Comment on the morphology of the red blood cells.
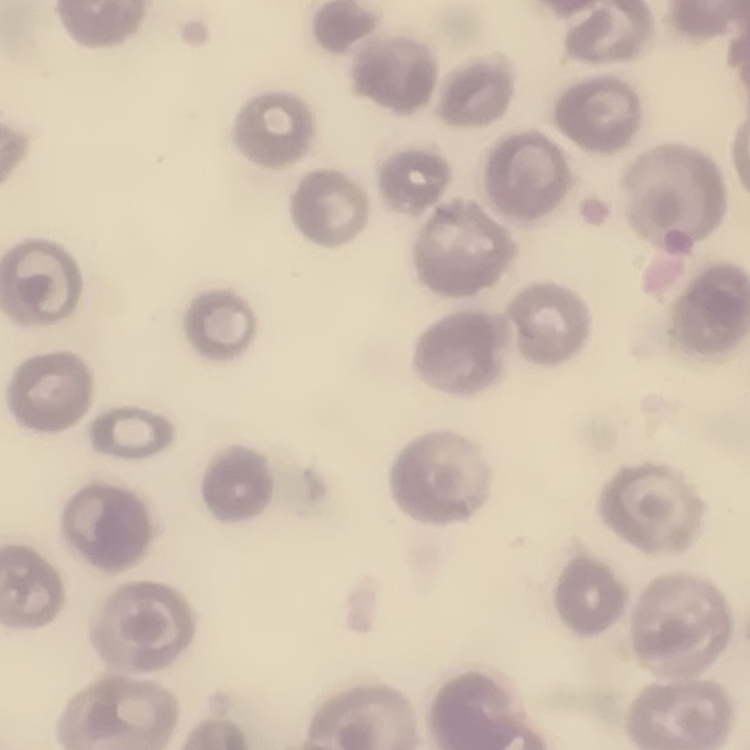
No rouleaux formation.

One tile cut from a larger photomicrograph. Field's or Giemsa stain. Thin blood smear.